Assess the morphology of the erythrocytes.
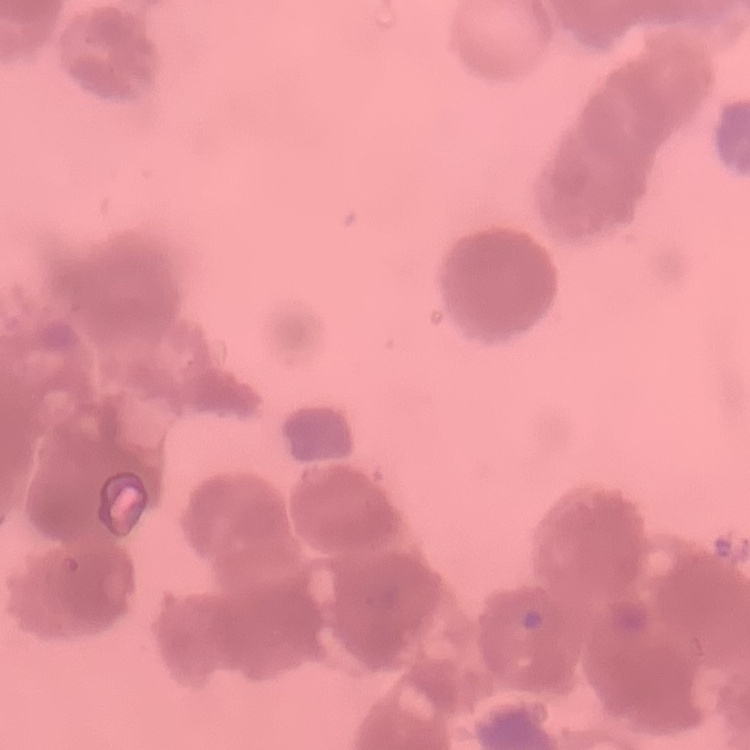
Rouleaux formation.

stain: Field's or Giemsa
preparation: thin blood film
image_type: square crop of a larger photomicrograph